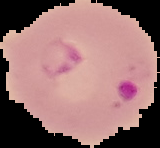
Summary:
  - Image size: 160×148 pixels
  - Result: malaria parasites detected
  - Preparation: thin blood smear
  - Image type: cell region segmented out of the field of view; surrounding area masked to black